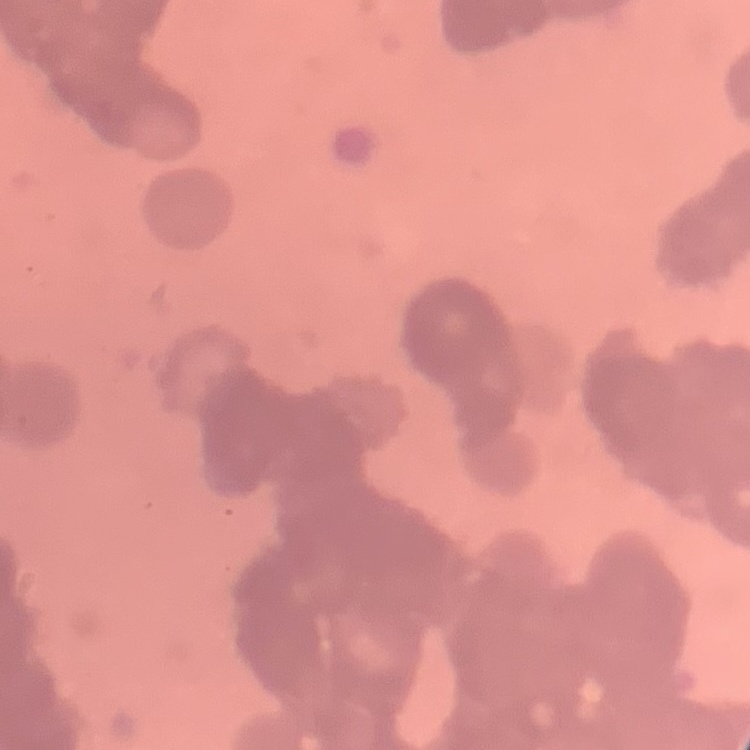
The red blood cells exhibit rouleaux formation. Thin blood film. Stained with either Field's or Giemsa. Square crop of a larger photomicrograph.